Locate every uninfected red blood cell.
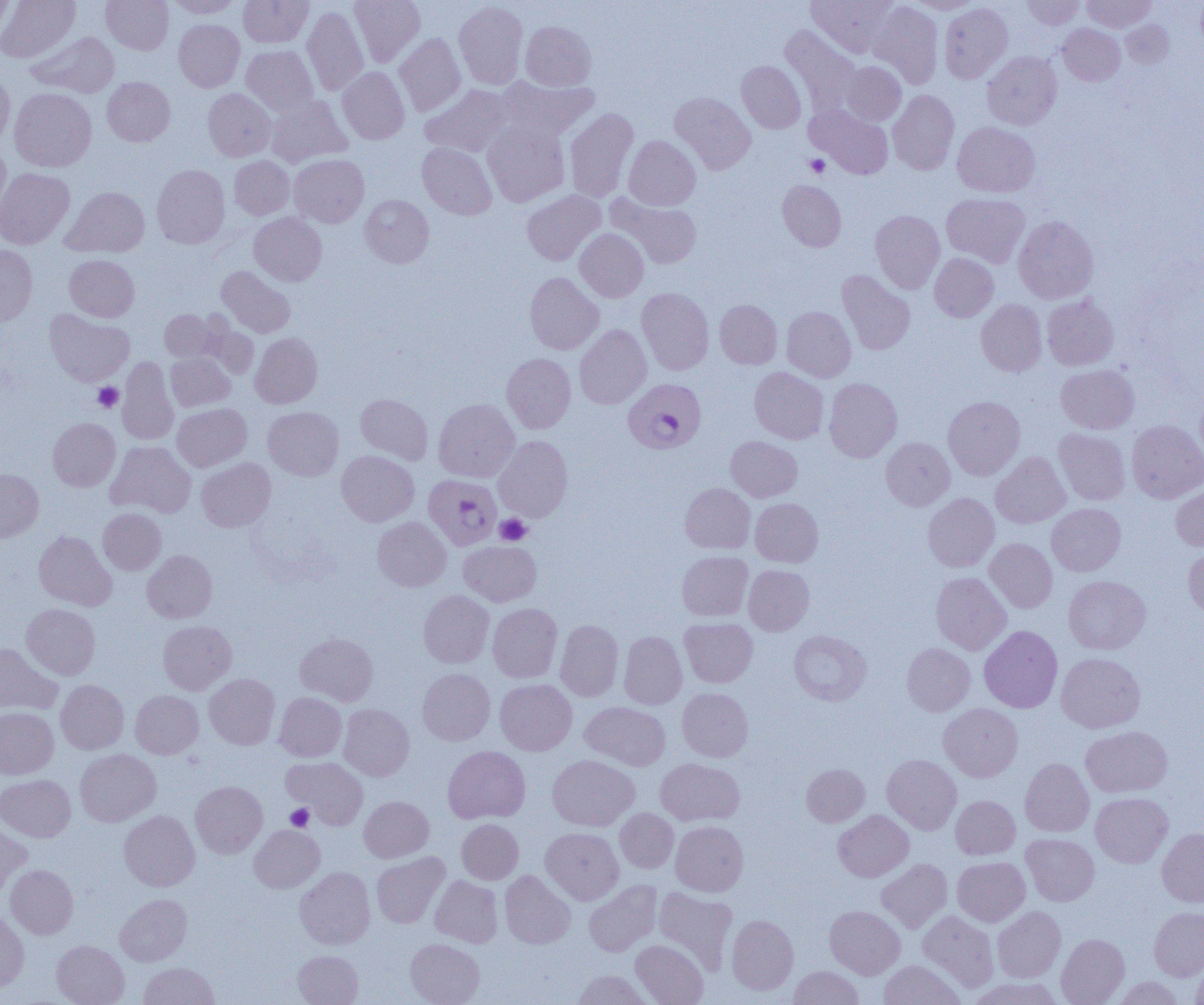
Approximate bounding boxes as (x1,y1)-(x2,y2) corner pairs in pixels.
Uninfected red blood cells: (0,0)-(14,39), (0,0)-(80,62), (101,0)-(174,54), (168,0)-(241,18), (239,0)-(313,48), (349,0)-(425,67), (807,0)-(895,56), (909,0)-(982,14), (1023,0)-(1084,29), (1082,0)-(1155,32), (454,1)-(528,89), (869,2)-(943,88), (939,3)-(1012,83), (302,6)-(368,96), (174,20)-(245,92), (1121,20)-(1173,68), (520,21)-(595,91), (1058,24)-(1125,85), (781,26)-(860,115), (28,32)-(120,98), (394,33)-(466,116), (241,45)-(319,116), (982,51)-(1062,130), (736,61)-(806,133), (840,61)-(906,125), (337,67)-(409,144), (0,72)-(14,149), (102,77)-(175,146), (497,77)-(598,143), (421,85)-(513,157), (10,88)-(96,172), (203,89)-(276,161), (888,90)-(959,175), (670,92)-(755,174), (266,96)-(351,167), (807,106)-(894,179), (564,108)-(638,202), (482,121)-(570,207), (952,122)-(1040,197), (624,136)-(701,210), (418,142)-(497,219), (0,143)-(10,218), (289,154)-(369,227), (229,156)-(294,220), (152,164)-(229,248), (0,168)-(74,249), (777,180)-(846,251), (62,186)-(149,257), (522,190)-(605,265), (942,193)-(1030,267), (360,195)-(434,267), (610,195)-(702,269), (870,210)-(945,293), (249,212)-(327,286), (1013,216)-(1098,303), (574,228)-(649,302), (0,245)-(37,326), (929,253)-(999,322), (64,255)-(139,322), (216,266)-(295,337), (837,270)-(915,355), (525,272)-(604,354), (636,287)-(714,375), (1042,294)-(1118,370), (715,299)-(782,369), (976,299)-(1046,376), (782,306)-(856,382), (44,309)-(134,386), (160,310)-(220,361), (199,323)-(259,379), (574,325)-(652,409), (250,332)-(322,408), (166,353)-(235,411), (502,353)-(576,433), (117,357)-(179,445), (1056,364)-(1139,434), (749,367)-(829,444), (824,378)-(902,462), (1195,388)-(1204,466), (356,394)-(433,464), (943,395)-(1025,480), (433,399)-(519,482), (172,403)-(251,471), (263,406)-(343,480), (48,418)-(120,491), (1127,420)-(1204,503), (1054,428)-(1130,505), (493,436)-(573,522), (726,436)-(802,501), (881,437)-(955,510), (106,441)-(196,517), (337,451)-(419,526), (991,451)-(1070,528), (196,458)-(275,532), (0,469)-(43,543), (1171,482)-(1204,550), (680,483)-(755,553), (923,493)-(999,572), (750,498)-(823,567), (1047,503)-(1125,576), (98,508)-(166,575), (373,517)-(451,591), (34,531)-(116,611), (984,538)-(1057,612), (459,540)-(541,607), (1183,546)-(1204,622), (142,550)-(217,623), (677,551)-(752,621), (743,565)-(814,635), (931,572)-(1011,655), (1063,575)-(1151,654), (418,590)-(493,668), (22,603)-(100,679), (488,603)-(562,682), (679,618)-(757,687), (555,619)-(623,701), (158,620)-(237,695), (979,626)-(1062,713), (788,630)-(871,706), (619,631)-(687,709), (295,633)-(378,706), (0,642)-(61,714), (902,643)-(975,716), (1056,652)-(1145,733), (418,668)-(495,745), (204,673)-(280,749), (55,679)-(128,754), (495,679)-(577,756), (677,687)-(753,762), (130,690)-(203,759), (274,692)-(347,761), (581,702)-(670,770), (939,703)-(1023,782), (338,704)-(414,781), (0,707)-(58,779), (1081,725)-(1173,797), (443,746)-(530,823), (75,749)-(161,826), (882,754)-(961,834), (548,755)-(638,831), (282,756)-(368,829), (656,758)-(744,826), (1020,758)-(1094,837), (801,764)-(869,826), (0,774)-(75,842), (190,781)-(267,857), (1091,792)-(1173,868), (950,795)-(1020,859), (359,796)-(434,862), (615,808)-(678,872), (119,810)-(199,891), (833,810)-(913,882), (456,819)-(523,884), (0,820)-(32,897), (671,821)-(748,896), (249,825)-(324,893), (541,827)-(624,905), (1156,828)-(1204,907), (1021,833)-(1099,906), (372,852)-(449,928), (952,857)-(1030,926), (876,859)-(952,933), (5,864)-(78,938), (295,867)-(375,949), (500,870)-(575,948), (430,876)-(503,947), (584,880)-(661,956), (653,887)-(737,974), (115,894)-(192,966), (825,905)-(905,979), (993,906)-(1066,982), (1149,907)-(1204,980), (0,910)-(29,991), (918,910)-(999,992), (727,915)-(798,995), (1056,934)-(1129,1005), (406,938)-(484,1005), (631,939)-(708,1004), (51,940)-(129,1005), (293,950)-(363,1005), (1191,957)-(1204,1005), (878,960)-(965,1005), (139,962)-(218,1005), (788,966)-(863,1005), (573,969)-(653,1005), (967,976)-(1063,1005), (1112,976)-(1184,1004).

Platelet locations: (805,154)-(830,178), (93,383)-(123,412), (495,514)-(531,546), (285,804)-(314,831). Plasmodium falciparum-infected red blood cell locations: (623,378)-(706,453), (423,475)-(501,550). Slide-level diagnosis: Plasmodium falciparum. Captured at 1000x magnification. Thin blood film. Image is 1204×1005 pixels. Light microscopy. Single field of view.